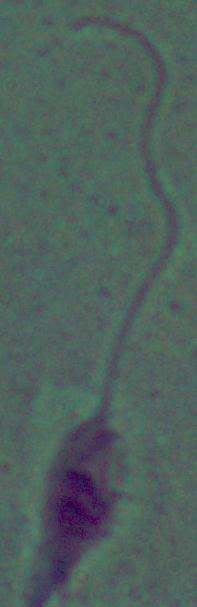
magnification = 1000x
identification = Leishmania
modality = photomicrograph